Mark where platelets are.
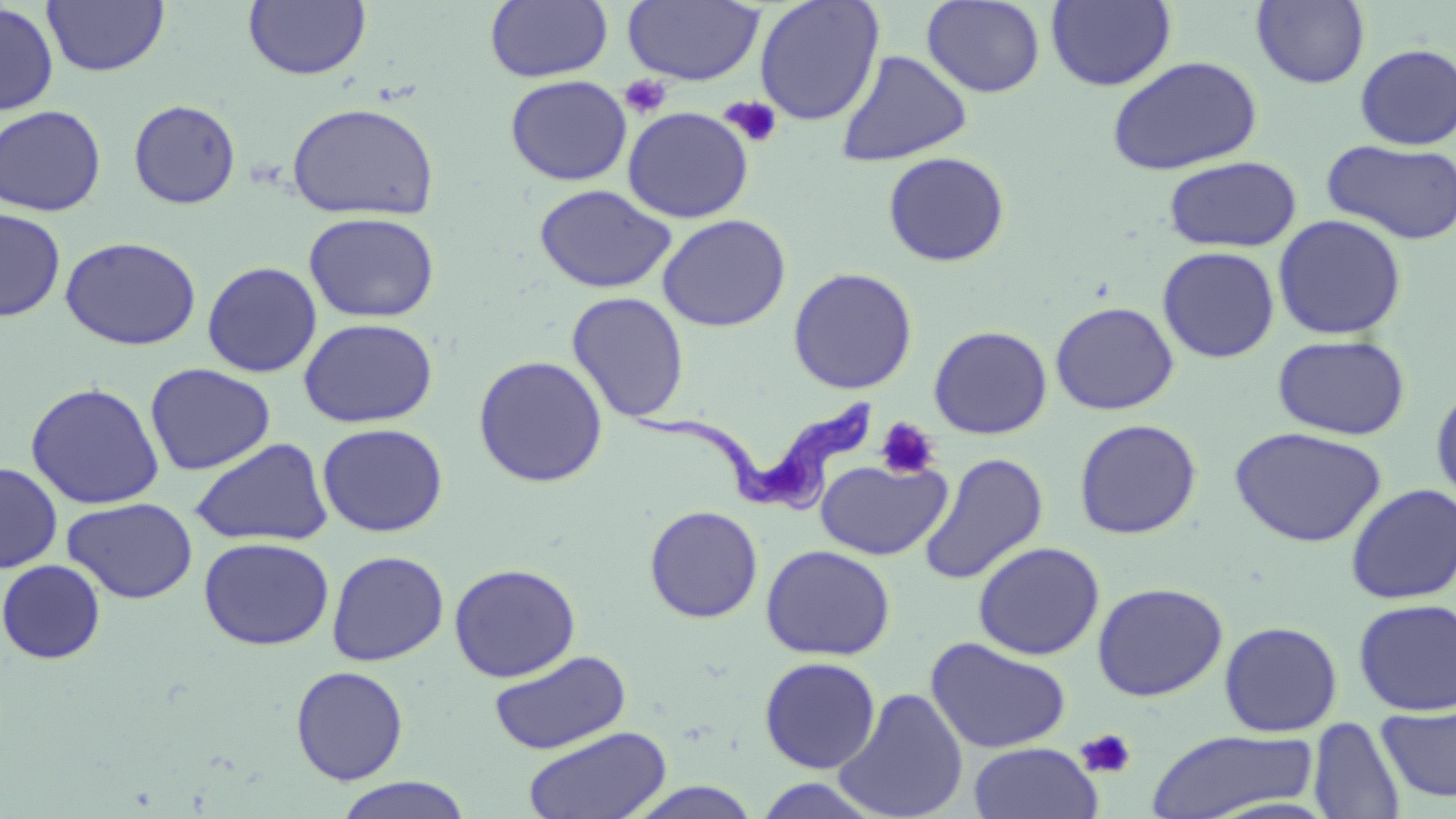
Approximate bounding boxes as [x1, y1, x2, y2] in pixels.
Platelets: [619, 74, 672, 119], [719, 95, 784, 149], [875, 417, 942, 480], [1075, 728, 1138, 780].

{
  "slide_level_diagnosis": "Trypanosoma brucei",
  "preparation": "thin blood film",
  "uninfected_red_blood_cell_locations": "approximate bounding boxes as [x1, y1, x2, y2] in pixels: [42, 0, 169, 77], [484, 0, 613, 83], [754, 0, 885, 126], [1046, 0, 1177, 91], [1251, 0, 1370, 89], [243, 1, 371, 81], [621, 1, 766, 85], [921, 1, 1046, 98], [1, 3, 59, 115], [1354, 43, 1456, 150], [836, 49, 972, 167], [1106, 55, 1263, 176], [505, 74, 632, 185], [128, 98, 242, 209], [285, 101, 440, 221], [0, 104, 107, 216], [622, 107, 754, 223], [1322, 139, 1456, 246], [882, 151, 1011, 267], [1163, 155, 1302, 253], [534, 184, 676, 294], [0, 208, 66, 322], [303, 211, 440, 323], [1272, 213, 1408, 340], [657, 214, 792, 332], [59, 236, 201, 351], [1157, 245, 1280, 364], [202, 261, 322, 377], [787, 267, 918, 395], [566, 292, 690, 423], [1050, 301, 1179, 415], [298, 317, 438, 428], [928, 325, 1053, 439], [1273, 333, 1411, 440], [472, 354, 609, 487], [144, 363, 276, 475], [1430, 380, 1456, 511], [25, 381, 165, 510], [1073, 418, 1202, 539], [317, 422, 448, 537], [1229, 426, 1387, 547], [189, 438, 334, 547], [917, 452, 1049, 586], [815, 458, 952, 560], [0, 462, 62, 573], [1345, 483, 1456, 605], [61, 497, 198, 604], [644, 504, 764, 624], [198, 536, 334, 650], [972, 541, 1106, 660], [760, 544, 896, 661], [326, 550, 449, 667], [0, 560, 106, 664], [448, 562, 581, 682], [1092, 581, 1229, 702], [1353, 598, 1456, 716], [1218, 620, 1343, 737], [925, 636, 1072, 754], [488, 649, 631, 755], [759, 656, 882, 773], [290, 665, 409, 786], [833, 687, 970, 819], [1376, 703, 1456, 805], [1307, 717, 1408, 819], [523, 725, 673, 819], [1145, 729, 1320, 819], [967, 742, 1105, 819], [749, 775, 889, 819], [334, 777, 472, 819]",
  "magnification": "1000x",
  "stain": "May-Grünwald-Giemsa",
  "field_of_view": "single",
  "image_size": "1456×819 pixels",
  "modality": "optical microscopy",
  "trypanosoma_brucei_locations": "approximate bounding boxes as [x1, y1, x2, y2] in pixels: [628, 397, 873, 514]"
}